Classify the preparation.
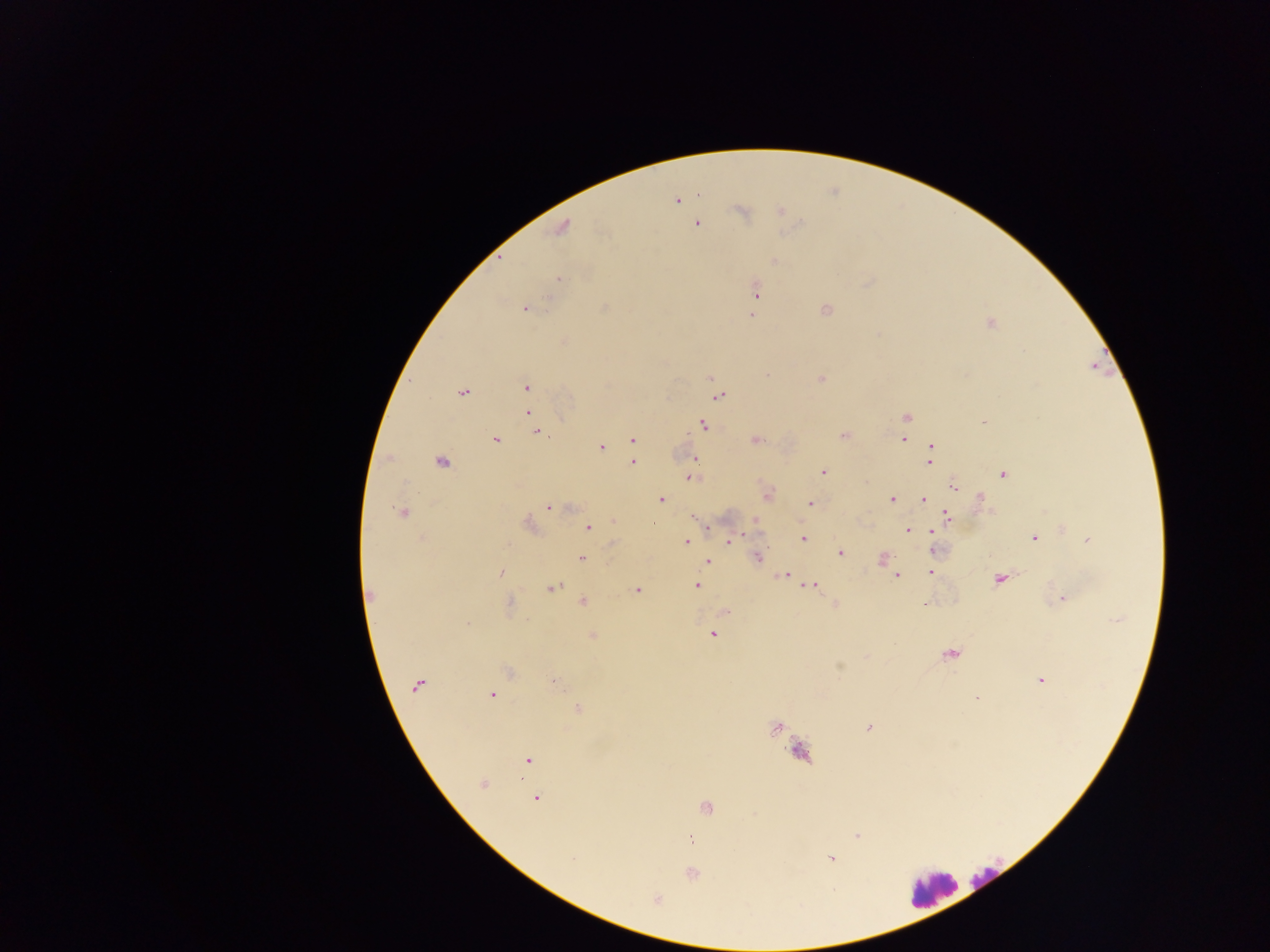

Thick blood smear.

Approximate centers as {x, y} in pixels. Plasmodium parasite locations: {676, 200}, {740, 211}, {780, 211}, {696, 224}, {562, 228}, {774, 261}, {558, 278}, {757, 292}, {525, 309}, {754, 309}, {825, 309}, {751, 315}, {989, 323}, {767, 374}, {711, 377}, {821, 379}, {526, 387}, {462, 393}, {719, 397}, {528, 413}, {906, 417}, {984, 421}, {704, 425}, {538, 431}, {843, 435}, {632, 439}, {903, 439}, {495, 440}, {755, 440}, {602, 447}, {931, 447}, {696, 459}, {930, 461}, {442, 462}, {634, 463}, {823, 472}, {1003, 474}, {690, 477}, {953, 487}, {767, 495}, {891, 499}, {981, 499}, {660, 500}, {924, 500}, {810, 504}, {548, 508}, {401, 512}, {694, 517}, {946, 517}, {613, 521}, {756, 522}, {527, 525}, {589, 528}, {708, 528}, {907, 531}, {932, 531}, {1034, 538}, {803, 539}, {614, 540}, {731, 540}, {1088, 540}, {686, 542}, {933, 550}, {840, 552}, {581, 558}, {757, 558}, {883, 559}, {707, 562}, {891, 570}, {501, 572}, {931, 572}, {785, 576}, {896, 577}, {999, 580}, {697, 585}, {811, 585}, {552, 588}, {637, 589}, {371, 595}, {1063, 599}, {583, 602}, {510, 604}, {923, 604}, {835, 605}, {726, 611}, {467, 625}, {712, 635}, {592, 636}, {950, 654}, {839, 666}, {509, 671}, {1041, 681}, {555, 683}, {417, 685}, {492, 696}, {976, 698}, {578, 709}, {774, 728}, {868, 728}, {527, 760}, {482, 784}, {537, 798}, {705, 807}, {857, 835}, {691, 839}, {831, 858}, {573, 859}, {692, 874}, {657, 898}. Leukocyte locations: {987, 879}, {930, 889}. Collected in Ghana. Mobile-phone photograph taken through the microscope. Image is 1270×952 pixels. Single field of view.